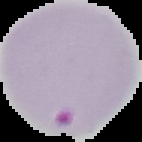
From a thin blood smear. The area outside the segmented cell region is set to black. Image is 142×142 pixels. Result: malaria parasites detected.